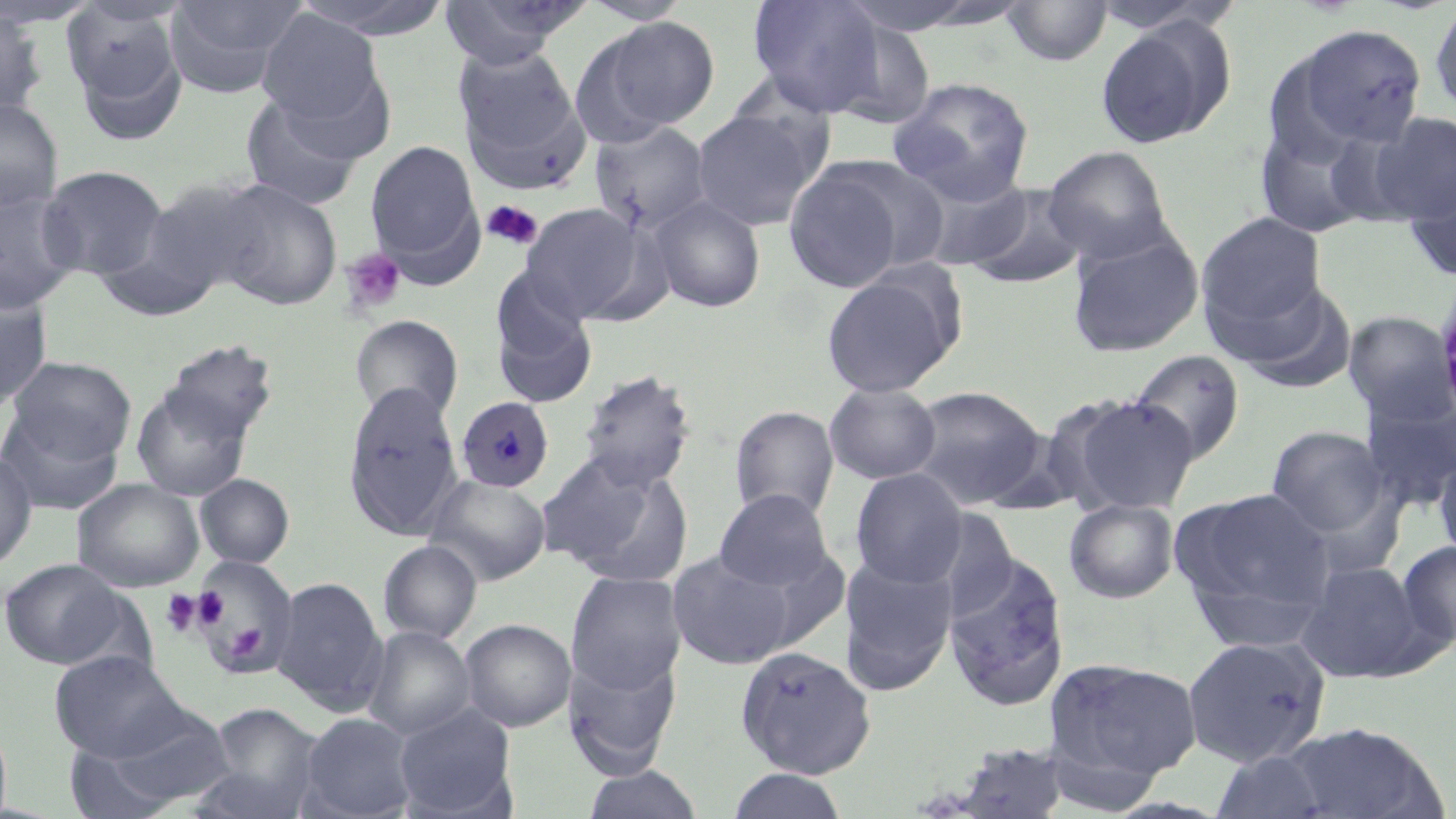

Summary:
  - Coordinate format: approximate bounding boxes as [x1, y1, x2, y2] in pixels
  - Platelet locations: [482, 200, 543, 250], [340, 248, 407, 316], [161, 588, 204, 637], [194, 588, 229, 630], [226, 623, 266, 661]
  - Uninfected red blood cell locations: [0, 0, 100, 28], [165, 0, 305, 96], [289, 0, 455, 41], [439, 0, 588, 69], [579, 0, 694, 25], [747, 0, 887, 117], [833, 0, 1002, 35], [62, 1, 188, 134], [1002, 1, 1113, 67], [1428, 2, 1456, 117], [0, 8, 48, 121], [257, 11, 383, 125], [593, 17, 722, 132], [1095, 20, 1233, 149], [1294, 24, 1429, 148], [454, 46, 580, 157], [888, 77, 1035, 203], [463, 89, 593, 198], [238, 91, 364, 210], [0, 97, 63, 214], [691, 109, 822, 231], [1367, 111, 1456, 224], [1255, 121, 1378, 239], [589, 122, 712, 236], [365, 139, 483, 272], [1043, 146, 1175, 264], [781, 159, 917, 294], [37, 165, 168, 280], [910, 168, 1035, 271], [1405, 176, 1456, 284], [212, 179, 343, 309], [964, 184, 1089, 290], [0, 188, 82, 313], [647, 194, 767, 313], [92, 201, 236, 322], [520, 202, 649, 322], [1196, 211, 1328, 334], [1066, 228, 1205, 358], [820, 269, 963, 398], [491, 278, 598, 406], [1229, 279, 1358, 394], [0, 281, 53, 414], [1342, 310, 1455, 426], [350, 314, 464, 423], [159, 338, 278, 448], [1127, 349, 1246, 465], [5, 355, 136, 463], [577, 369, 696, 492], [131, 382, 253, 501], [824, 382, 941, 484], [343, 383, 464, 540], [905, 385, 1049, 510], [1358, 393, 1456, 513], [1060, 394, 1200, 516], [729, 405, 840, 523], [0, 409, 124, 515], [1266, 425, 1391, 538], [1433, 443, 1456, 570], [0, 448, 38, 572], [541, 452, 695, 587], [849, 469, 967, 588], [195, 473, 294, 568], [424, 474, 552, 586], [73, 478, 204, 593], [1174, 486, 1336, 626], [714, 489, 836, 592], [1063, 498, 1179, 603], [922, 507, 1020, 621], [1396, 539, 1456, 653], [378, 540, 483, 644], [668, 549, 799, 671], [943, 551, 1071, 709], [838, 555, 959, 695], [0, 558, 129, 670], [1296, 558, 1426, 683], [566, 571, 686, 695], [271, 576, 387, 713], [459, 618, 575, 732], [363, 626, 475, 741], [1181, 636, 1331, 767], [734, 645, 877, 779], [563, 647, 682, 776], [49, 650, 190, 762], [1045, 657, 1203, 785], [200, 702, 325, 816], [394, 704, 517, 818], [76, 708, 237, 814], [298, 713, 417, 819], [1279, 721, 1449, 817], [62, 739, 187, 819], [932, 740, 1072, 818], [1210, 749, 1335, 818], [581, 765, 706, 819], [725, 769, 850, 819]
  - Plasmodium malariae-infected red blood cell locations: [456, 396, 554, 492]
  - Slide-level diagnosis: Plasmodium malariae
  - Field of view: one of a larger specimen
  - Stain: May-Grünwald-Giemsa
  - Magnification: 1000x
  - Image size: 1456×819 pixels
  - Modality: light microscopy
  - Preparation: thin blood smear